Report the malaria status of this cell.
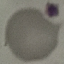

It is uninfected.

Summary:
  - Preparation: thin smear
  - Stain: Giemsa
  - Image type: automatically extracted cell patch, resized to 64 × 64 pixels
  - Capture: smartphone through the microscope eyepiece